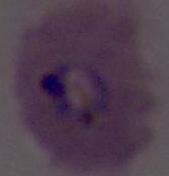

Summary:
  - Magnification: 400x or 1000x
  - Modality: micrograph
  - Identification: Plasmodium